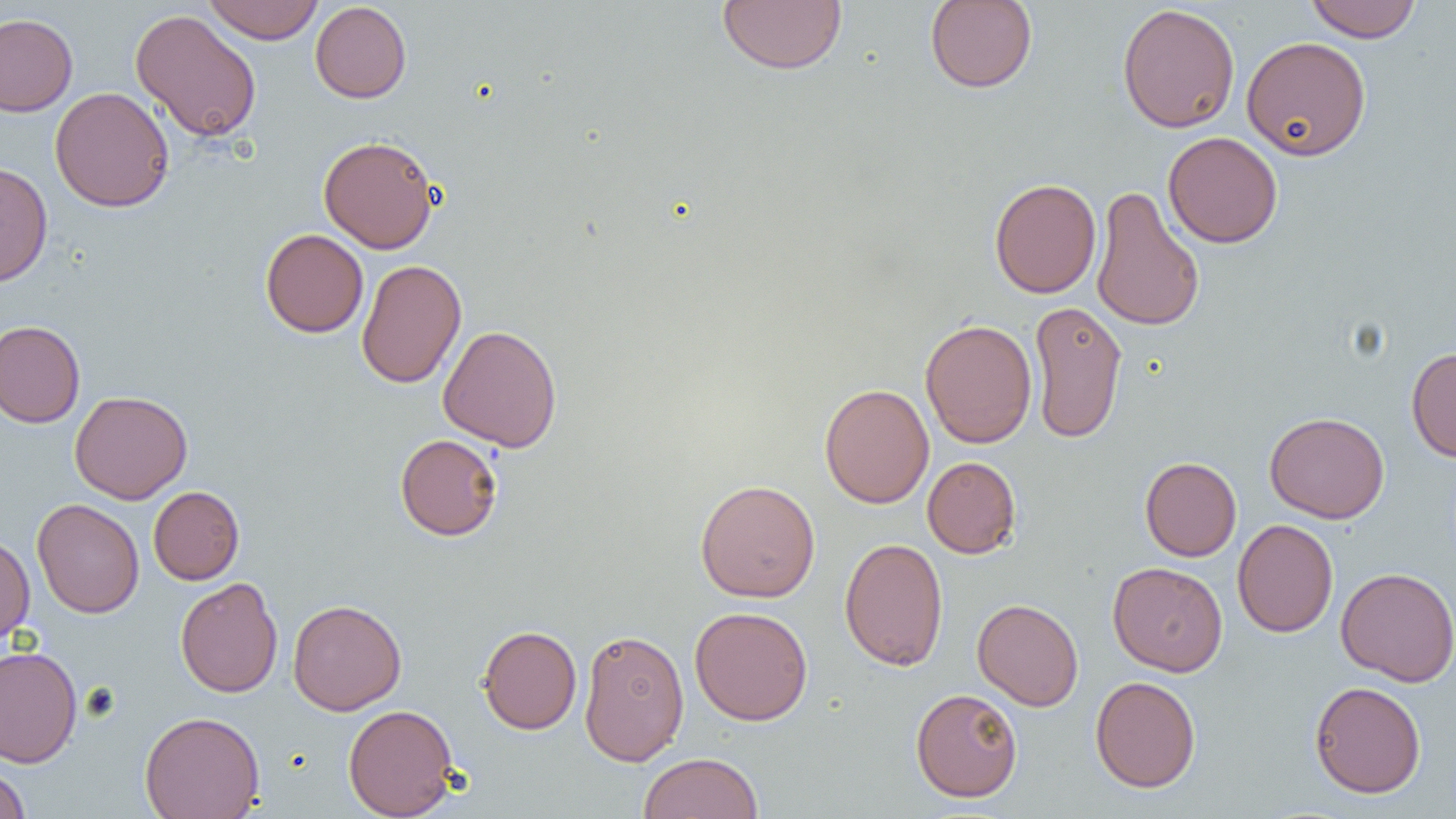
Approximate bounding boxes as (x1,y1)-(x2,y2) corner pairs in pixels. Uninfected red blood cell locations: (202,0)-(324,44), (1305,0)-(1421,42), (310,1)-(411,103), (717,1)-(846,74), (925,1)-(1038,93), (1116,3)-(1240,133), (130,9)-(262,143), (0,13)-(78,116), (1241,36)-(1371,161), (50,86)-(174,213), (1163,131)-(1283,248), (318,135)-(440,253), (0,161)-(53,287), (989,178)-(1101,298), (1090,184)-(1205,334), (260,229)-(368,338), (356,258)-(466,389), (1028,299)-(1128,445), (920,318)-(1037,449), (0,320)-(85,428), (438,324)-(562,452), (1406,346)-(1456,462), (819,383)-(934,508), (69,390)-(193,504), (1264,412)-(1390,523), (395,434)-(503,540), (922,456)-(1021,558), (1140,457)-(1241,561), (695,479)-(820,602), (148,486)-(244,585), (31,498)-(144,618), (1232,519)-(1338,638), (0,533)-(35,647), (839,536)-(949,672), (1107,561)-(1228,676), (1335,566)-(1456,687), (175,577)-(283,698), (972,598)-(1084,711), (288,599)-(406,715), (689,606)-(813,725), (478,625)-(582,734), (578,628)-(689,766), (0,645)-(82,768), (1090,675)-(1201,793), (1310,681)-(1426,798), (910,687)-(1023,802), (343,703)-(459,818), (139,711)-(265,819), (639,752)-(763,819), (0,762)-(31,819). Slide-level diagnosis: negative for blood parasites. One field of a larger specimen. Captured at 1000x magnification. Optical microscopy. Image is 1456×819 pixels. Thin blood film.